Report the malaria status of this cell.
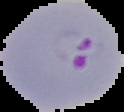
Parasitized.

Image is 124×112 pixels. The area outside the segmented cell region is set to black. From a thin blood smear.